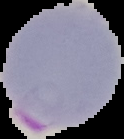

{
  "preparation": "thin blood film",
  "image_size": "124×139 pixels",
  "result": "Plasmodium parasites identified",
  "image_type": "cell region segmented out of the field of view; surrounding area masked to black"
}